Identify the parasite.
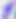

Toxoplasma gondii.

Summary:
  - Magnification: 400x
  - Modality: photomicrograph